Give the position of every leukocyte visible.
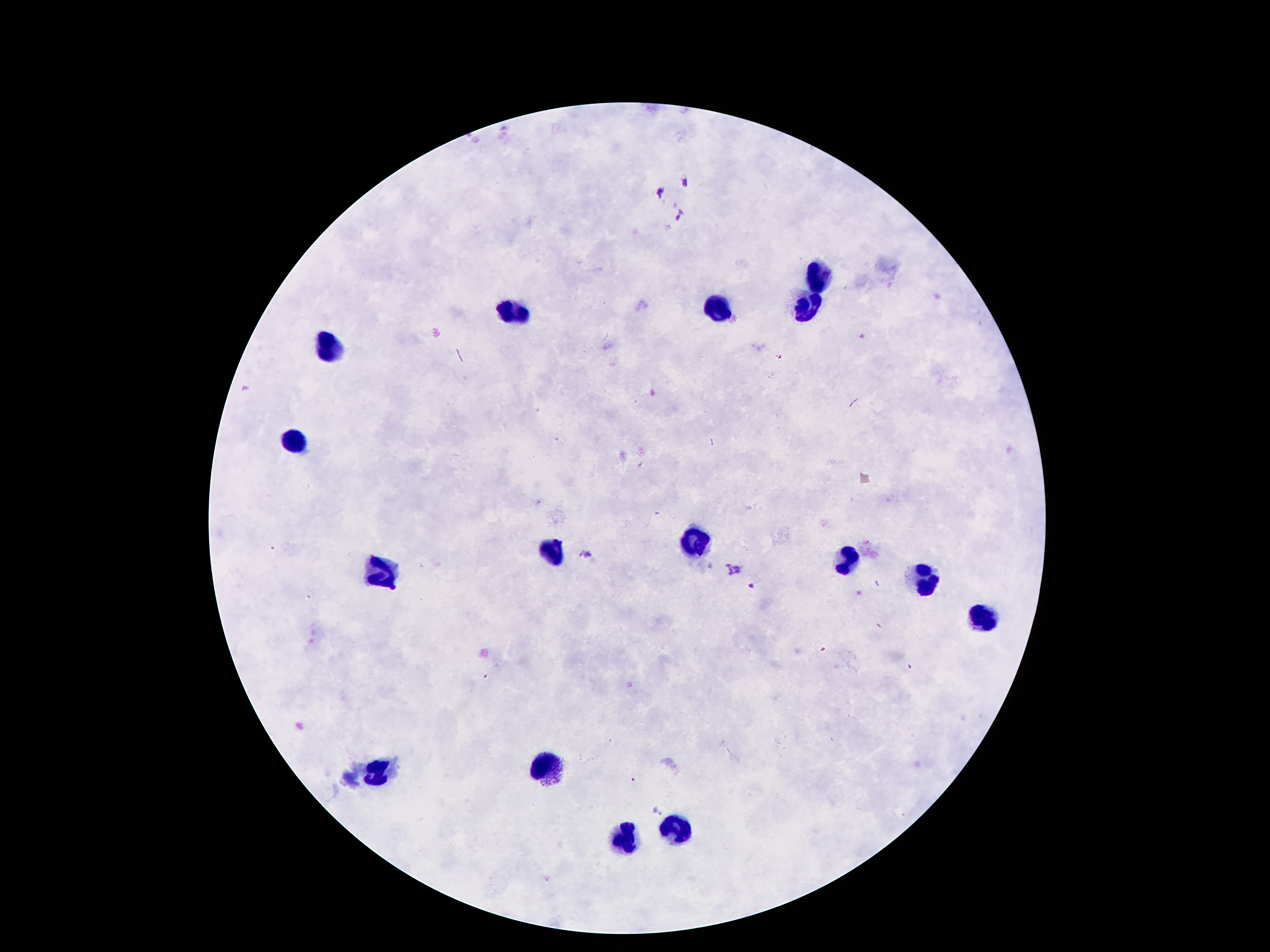

Approximate centers as {x, y} in pixels.
Leukocytes: {815, 277}, {805, 310}, {719, 311}, {512, 314}, {332, 350}, {293, 443}, {697, 543}, {553, 554}, {844, 560}, {379, 571}, {926, 582}, {983, 622}, {547, 770}, {377, 771}, {676, 827}, {627, 837}.

{
  "patient_malaria_status": "not infected",
  "magnification": "100x",
  "preparation": "thick blood smear",
  "field_of_view": "single",
  "capture": "smartphone camera through the microscope eyepiece",
  "image_size": "1270×952 pixels",
  "stain": "Giemsa"
}